Report the malaria status of this cell.
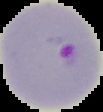
Parasitized.

Segmented cell region on a black background. Image is 103×112 pixels. From a thin blood smear.